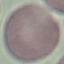
Summary:
  - Result: no malaria parasites seen
  - Image type: automatically extracted cell patch, resized to 64 × 64 pixels
  - Stain: Giemsa
  - Preparation: thin blood smear
  - Capture: smartphone camera at the microscope eyepiece